Identify the parasite.
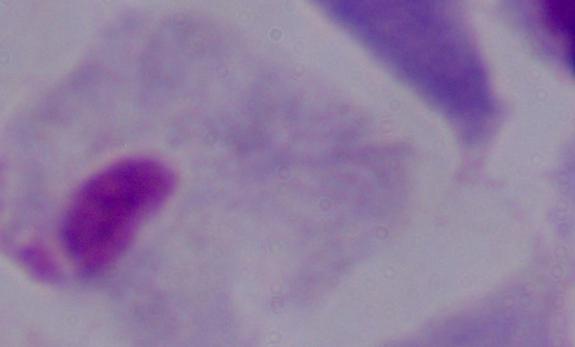

This is a trichomonad.

Summary:
  - Magnification: 1000x
  - Modality: photomicrograph